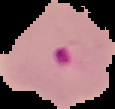

Summary:
  - Preparation: thin blood film
  - Result: malaria parasites detected
  - Image size: 115×109 pixels
  - Image type: cell region segmented out of the field of view; surrounding area masked to black